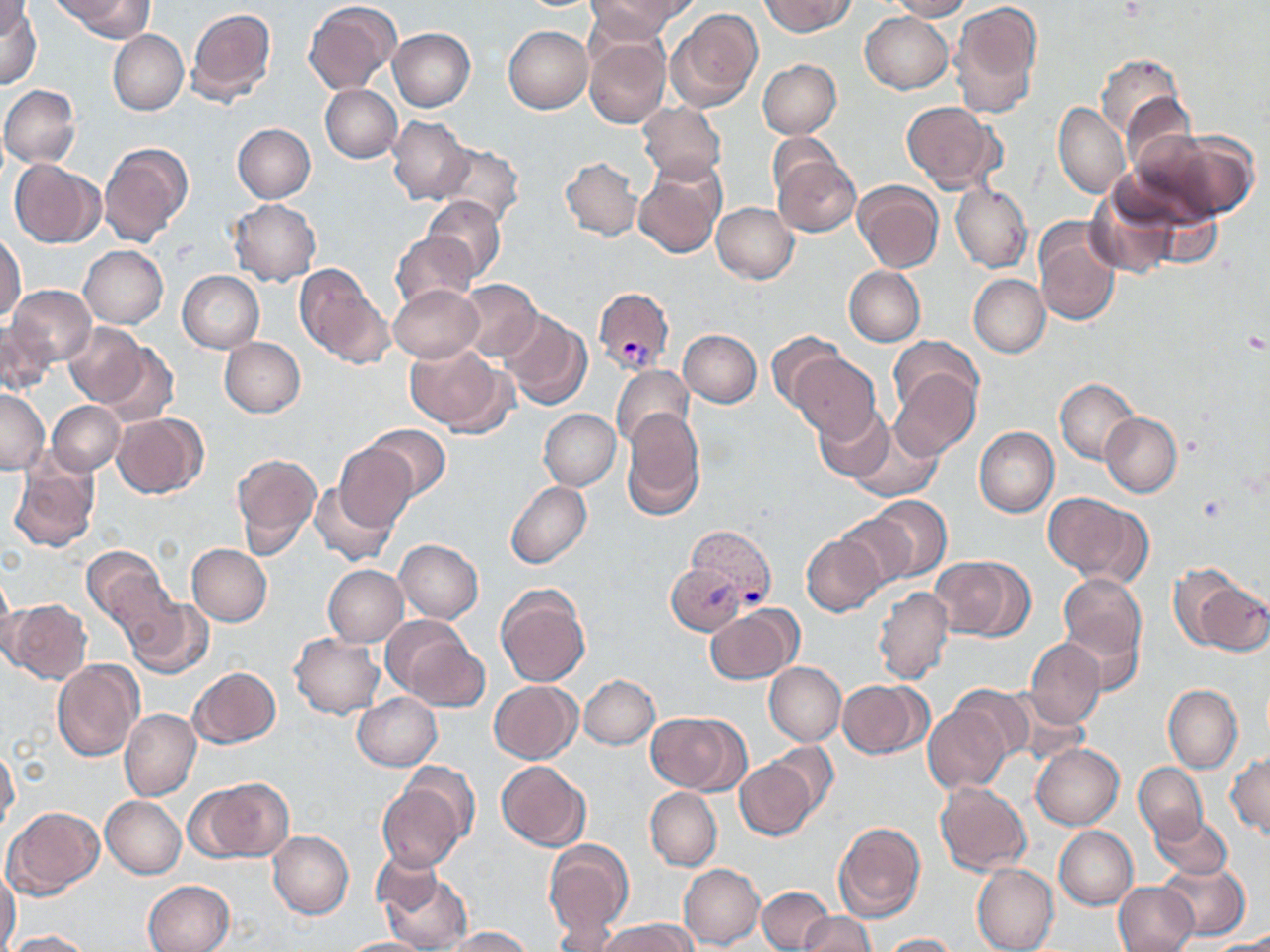
Approximate bounding boxes as named x1/y1/x2/y2 corners in pixels. Uninfected red blood cell locations: (x1=56, y1=0, x2=151, y2=40), (x1=587, y1=0, x2=688, y2=40), (x1=758, y1=0, x2=855, y2=36), (x1=884, y1=0, x2=972, y2=20), (x1=1, y1=1, x2=33, y2=42), (x1=304, y1=1, x2=401, y2=94), (x1=0, y1=2, x2=42, y2=90), (x1=948, y1=2, x2=1041, y2=119), (x1=185, y1=6, x2=276, y2=106), (x1=667, y1=9, x2=762, y2=111), (x1=860, y1=11, x2=954, y2=94), (x1=503, y1=25, x2=593, y2=114), (x1=389, y1=27, x2=475, y2=111), (x1=583, y1=29, x2=670, y2=131), (x1=108, y1=30, x2=188, y2=114), (x1=1097, y1=53, x2=1187, y2=141), (x1=757, y1=59, x2=840, y2=139), (x1=321, y1=84, x2=401, y2=163), (x1=1, y1=85, x2=81, y2=167), (x1=637, y1=101, x2=727, y2=182), (x1=902, y1=102, x2=1002, y2=193), (x1=1053, y1=103, x2=1129, y2=199), (x1=388, y1=115, x2=473, y2=204), (x1=232, y1=123, x2=315, y2=202), (x1=1132, y1=126, x2=1258, y2=222), (x1=768, y1=131, x2=839, y2=199), (x1=99, y1=143, x2=193, y2=245), (x1=434, y1=144, x2=524, y2=227), (x1=773, y1=156, x2=861, y2=237), (x1=8, y1=158, x2=104, y2=247), (x1=561, y1=158, x2=642, y2=241), (x1=632, y1=162, x2=724, y2=259), (x1=853, y1=179, x2=943, y2=272), (x1=951, y1=183, x2=1032, y2=273), (x1=1085, y1=188, x2=1183, y2=279), (x1=422, y1=196, x2=505, y2=282), (x1=229, y1=199, x2=321, y2=286), (x1=711, y1=203, x2=799, y2=284), (x1=1033, y1=220, x2=1122, y2=327), (x1=391, y1=231, x2=476, y2=310), (x1=1, y1=232, x2=26, y2=320), (x1=79, y1=246, x2=168, y2=328), (x1=293, y1=263, x2=392, y2=369), (x1=844, y1=266, x2=925, y2=347), (x1=177, y1=270, x2=265, y2=354), (x1=969, y1=273, x2=1051, y2=357), (x1=455, y1=280, x2=542, y2=359), (x1=388, y1=283, x2=483, y2=363), (x1=9, y1=285, x2=96, y2=366), (x1=500, y1=310, x2=592, y2=410), (x1=1, y1=321, x2=55, y2=396), (x1=63, y1=322, x2=147, y2=406), (x1=677, y1=328, x2=762, y2=408), (x1=765, y1=331, x2=844, y2=416), (x1=219, y1=337, x2=305, y2=417), (x1=889, y1=337, x2=982, y2=419), (x1=96, y1=341, x2=179, y2=427), (x1=406, y1=344, x2=513, y2=437), (x1=788, y1=353, x2=881, y2=444), (x1=889, y1=363, x2=980, y2=460), (x1=612, y1=365, x2=695, y2=452), (x1=1055, y1=379, x2=1140, y2=465), (x1=0, y1=388, x2=50, y2=475), (x1=46, y1=401, x2=125, y2=475), (x1=814, y1=404, x2=893, y2=482), (x1=539, y1=408, x2=621, y2=490), (x1=622, y1=409, x2=706, y2=520), (x1=113, y1=413, x2=207, y2=498), (x1=1100, y1=413, x2=1182, y2=498), (x1=848, y1=416, x2=943, y2=501), (x1=366, y1=425, x2=450, y2=502), (x1=974, y1=427, x2=1059, y2=517), (x1=334, y1=443, x2=418, y2=531), (x1=231, y1=453, x2=321, y2=557), (x1=8, y1=458, x2=100, y2=552), (x1=505, y1=480, x2=591, y2=569), (x1=309, y1=481, x2=397, y2=566), (x1=1043, y1=494, x2=1150, y2=584), (x1=868, y1=496, x2=952, y2=580), (x1=836, y1=509, x2=920, y2=589), (x1=801, y1=533, x2=887, y2=615), (x1=394, y1=539, x2=484, y2=623), (x1=187, y1=543, x2=271, y2=626), (x1=81, y1=546, x2=170, y2=628), (x1=928, y1=556, x2=1030, y2=640), (x1=665, y1=564, x2=750, y2=635), (x1=323, y1=565, x2=408, y2=646), (x1=0, y1=567, x2=15, y2=659), (x1=1058, y1=573, x2=1146, y2=664), (x1=1184, y1=574, x2=1270, y2=655), (x1=496, y1=584, x2=591, y2=686), (x1=872, y1=585, x2=953, y2=685), (x1=123, y1=597, x2=212, y2=679), (x1=4, y1=599, x2=92, y2=684), (x1=705, y1=606, x2=801, y2=684), (x1=383, y1=617, x2=487, y2=712), (x1=1061, y1=618, x2=1143, y2=696), (x1=289, y1=634, x2=384, y2=718), (x1=1026, y1=638, x2=1107, y2=728), (x1=51, y1=658, x2=145, y2=762), (x1=764, y1=662, x2=845, y2=745), (x1=187, y1=667, x2=280, y2=748), (x1=579, y1=674, x2=659, y2=749), (x1=836, y1=679, x2=929, y2=758), (x1=488, y1=681, x2=582, y2=764), (x1=1163, y1=684, x2=1242, y2=773), (x1=950, y1=686, x2=1035, y2=766), (x1=994, y1=688, x2=1091, y2=769), (x1=352, y1=693, x2=442, y2=770), (x1=923, y1=702, x2=1011, y2=793), (x1=120, y1=708, x2=201, y2=801), (x1=645, y1=712, x2=748, y2=793), (x1=765, y1=737, x2=839, y2=817), (x1=1031, y1=744, x2=1123, y2=830), (x1=0, y1=748, x2=19, y2=834), (x1=1227, y1=753, x2=1270, y2=840), (x1=734, y1=756, x2=818, y2=840), (x1=395, y1=761, x2=480, y2=844), (x1=497, y1=761, x2=590, y2=850), (x1=1133, y1=763, x2=1208, y2=841), (x1=189, y1=779, x2=292, y2=862), (x1=933, y1=781, x2=1032, y2=876), (x1=376, y1=782, x2=466, y2=873), (x1=646, y1=787, x2=722, y2=871), (x1=101, y1=797, x2=186, y2=878), (x1=3, y1=806, x2=105, y2=899), (x1=1151, y1=812, x2=1233, y2=880), (x1=834, y1=822, x2=925, y2=923), (x1=1054, y1=826, x2=1138, y2=910), (x1=267, y1=830, x2=354, y2=919), (x1=543, y1=840, x2=633, y2=946), (x1=373, y1=848, x2=445, y2=917), (x1=1157, y1=861, x2=1249, y2=941), (x1=679, y1=863, x2=765, y2=950), (x1=972, y1=864, x2=1059, y2=952), (x1=0, y1=867, x2=21, y2=950), (x1=379, y1=869, x2=473, y2=952), (x1=143, y1=880, x2=234, y2=952), (x1=1113, y1=881, x2=1197, y2=952), (x1=758, y1=887, x2=832, y2=950), (x1=800, y1=912, x2=876, y2=952), (x1=596, y1=918, x2=695, y2=951), (x1=439, y1=926, x2=535, y2=951), (x1=7, y1=930, x2=97, y2=952), (x1=883, y1=932, x2=958, y2=951), (x1=337, y1=937, x2=436, y2=951), (x1=1203, y1=940, x2=1270, y2=952). Plasmodium vivax-infected red blood cell locations: (x1=594, y1=287, x2=674, y2=374), (x1=686, y1=525, x2=777, y2=605). Platelet locations: (x1=1243, y1=329, x2=1267, y2=352), (x1=1196, y1=495, x2=1226, y2=524). Slide-level diagnosis: Plasmodium vivax. Single field of view. May-Grünwald-Giemsa stain. Thin blood film. Optical microscopy. Image is 1270×952 pixels. Captured at 1000x magnification.